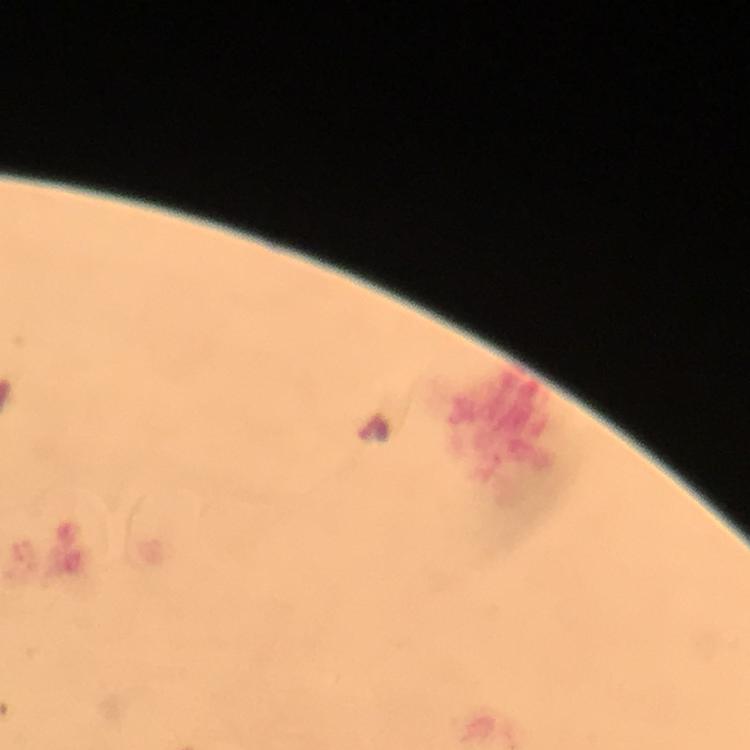

{
  "magnification": "100x",
  "stain": "Giemsa",
  "cropped_from": "a single field of view",
  "context": "from a malaria diagnostic workup",
  "preparation": "thick blood film",
  "leukocyte_locations": "approximate object centers, in pixels from the top-left corner: (x=500, y=430)",
  "plasmodium_parasite_locations": "approximate object centers, in pixels from the top-left corner: (x=372, y=427)",
  "capture": "smartphone photograph through a microscope",
  "image_size": "750×750 pixels",
  "immersion_oil": "applied"
}